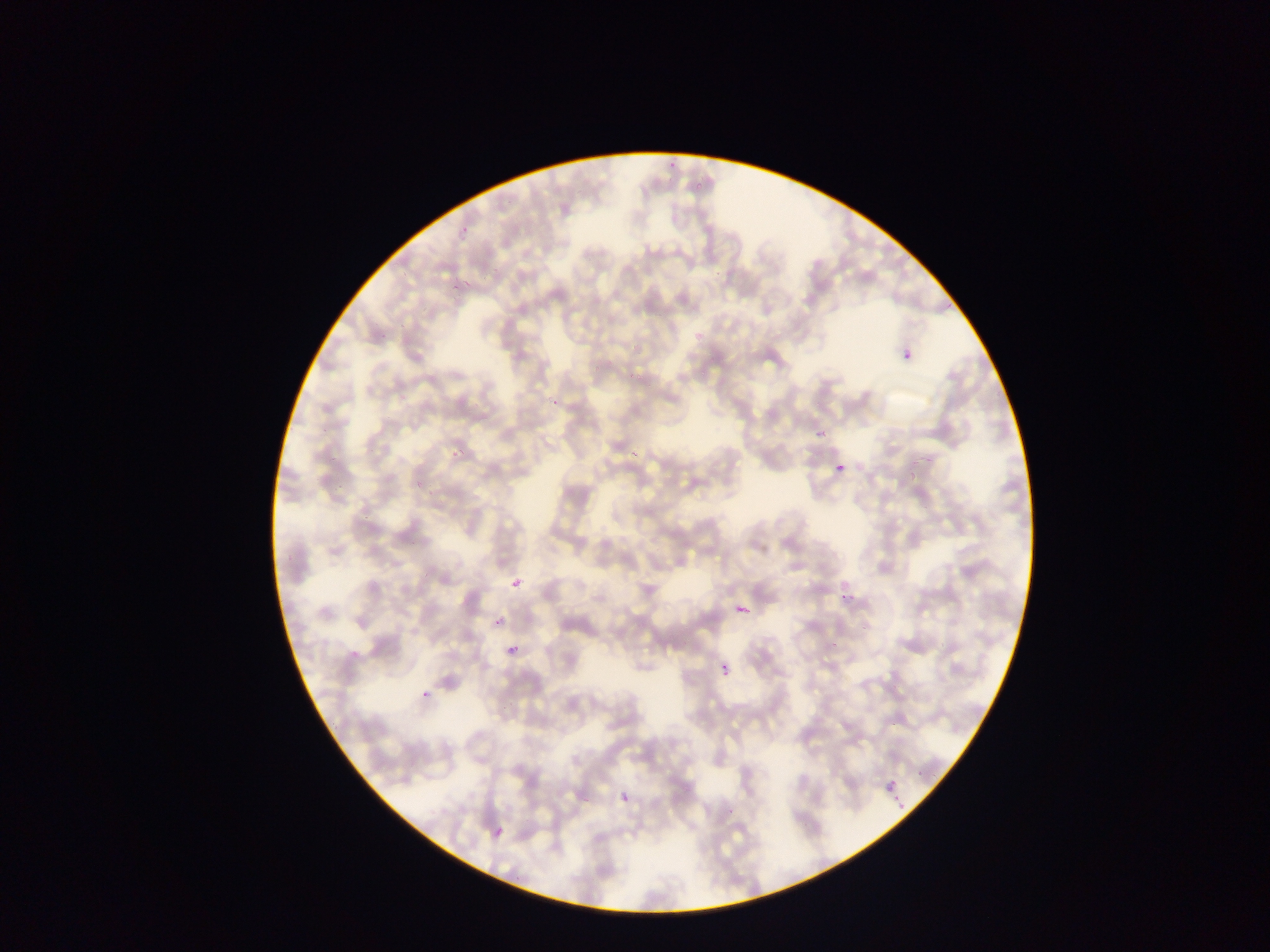

Plasmodium parasite locations = approximate bounding boxes as left top right bottom in pixels: 455 219 467 242; 449 280 468 294; 898 334 919 357; 547 395 560 409; 809 426 823 443; 450 438 471 461; 625 444 636 461; 834 465 851 482; 509 574 521 591; 844 585 861 597; 733 598 762 618; 490 615 507 632; 506 632 526 661; 715 665 731 677; 416 684 439 707; 880 771 905 796; 617 795 627 805; 888 795 909 816; 486 822 500 840
preparation = thin blood smear
country = Ghana
field of view = single
image size = 1270×952 pixels
capture = mobile-phone photograph through a microscope